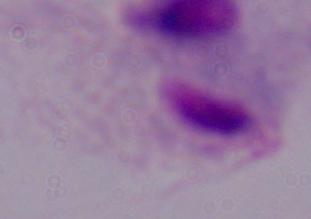 Captured at 1000x magnification. Micrograph. A trichomonad is shown.